Locate every blood parasite and identify its species.
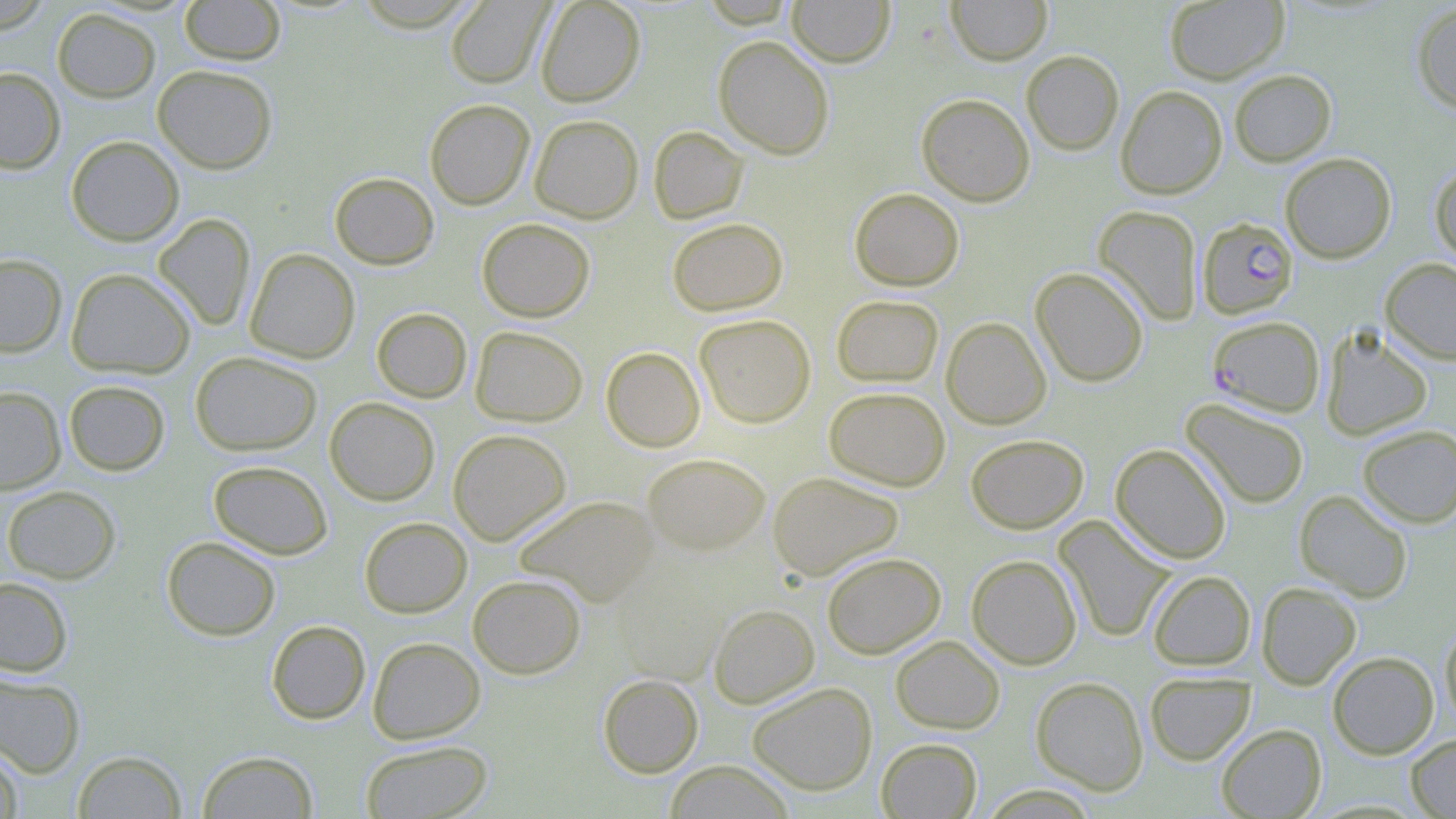

Approximate bounding boxes as (x1, y1, x2, y2) in pixels.
Plasmodium falciparum-infected red blood cells: (1197, 217, 1298, 318), (1211, 318, 1330, 419).
No Plasmodium ovale, Plasmodium malariae, Plasmodium vivax, Babesia divergens, or Trypanosoma brucei observed.

Uninfected red blood cell locations: (179, 0, 286, 65), (534, 0, 646, 107), (787, 0, 895, 67), (946, 0, 1052, 65), (445, 1, 552, 88), (1164, 1, 1290, 84), (1411, 2, 1456, 115), (52, 8, 160, 102), (713, 35, 835, 159), (1021, 50, 1124, 155), (152, 65, 278, 174), (0, 67, 66, 174), (1229, 69, 1337, 166), (1115, 85, 1228, 199), (916, 93, 1035, 206), (424, 98, 535, 210), (529, 114, 643, 223), (648, 125, 749, 224), (65, 135, 184, 246), (1280, 152, 1397, 264), (1430, 162, 1456, 267), (329, 172, 439, 270), (849, 187, 964, 291), (1093, 205, 1203, 325), (153, 213, 256, 331), (667, 217, 788, 316), (477, 218, 595, 322), (245, 248, 360, 363), (0, 253, 67, 357), (1379, 257, 1456, 365), (1030, 267, 1149, 387), (66, 268, 195, 379), (831, 294, 944, 387), (371, 307, 472, 403), (694, 314, 816, 428), (941, 316, 1051, 429), (470, 326, 588, 426), (1320, 326, 1433, 440), (601, 346, 705, 452), (190, 351, 321, 456), (63, 380, 170, 476), (0, 386, 66, 494), (824, 386, 950, 490), (324, 397, 440, 505), (1181, 398, 1310, 509), (1356, 424, 1456, 527), (448, 429, 571, 545), (965, 434, 1089, 533), (1110, 443, 1232, 564), (642, 453, 770, 556), (208, 460, 333, 559), (767, 471, 903, 581), (2, 485, 120, 583), (1294, 490, 1413, 602), (514, 495, 659, 605), (359, 516, 472, 618), (1054, 516, 1175, 643), (161, 536, 281, 641), (822, 552, 946, 658), (966, 554, 1082, 670), (611, 568, 726, 686), (1148, 570, 1255, 670), (467, 574, 586, 678), (0, 576, 73, 676), (1256, 581, 1362, 690), (708, 604, 820, 708), (266, 620, 370, 724), (1440, 622, 1456, 729), (890, 635, 1005, 734), (368, 636, 486, 744), (1327, 651, 1439, 759), (0, 670, 86, 778), (1144, 671, 1256, 765), (597, 674, 704, 777), (1030, 676, 1148, 794), (747, 682, 878, 795), (1216, 724, 1327, 818), (1405, 733, 1456, 818), (876, 738, 983, 818), (360, 740, 493, 819), (0, 744, 23, 819), (72, 750, 186, 818), (197, 750, 319, 818), (665, 761, 794, 818). Slide-level diagnosis: Plasmodium falciparum. May-Grünwald-Giemsa stain. Optical microscopy. Image is 1456×819 pixels. Captured at 1000x magnification. Single field of view. Thin blood smear.